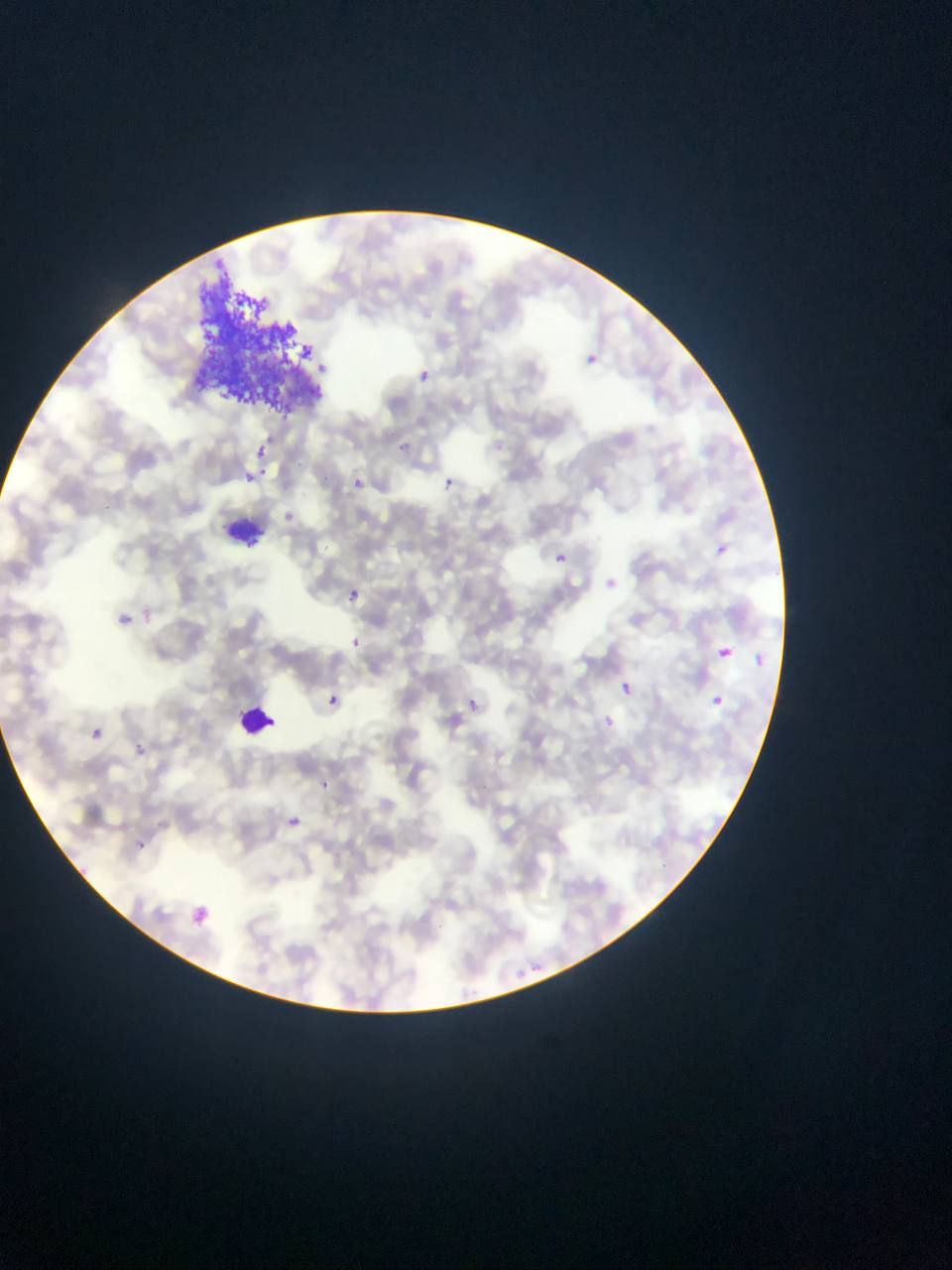
plasmodium_parasite_locations: 'approximate bounding boxes as left top right bottom in pixels: 584 354 601 371; 417 368 432 383; 402 435 419 452; 252 443 269 460; 242 472 257 485; 351 477 363 489; 443 477 454 488; 281 511 298 525; 711 541 730 559; 555 553 568 565; 346 588 361 603; 117 612 127 625; 347 636 363 651; 717 647 730 660; 753 654 767 668; 619 683 633 696; 322 692 344 711; 470 694 486 721; 713 696 724 706; 602 716 614 727; 85 724 106 745; 134 737 151 760; 318 780 346 798; 279 811 307 835; 129 836 150 856; 185 903 213 929'
artifact_stain_precipitate_or_debris_locations: 'approximate bounding boxes as left top right bottom in pixels: 200 271 319 415'
capture: mobile-phone photograph through a microscope
leukocyte_locations: 'approximate bounding boxes as left top right bottom in pixels: 223 511 266 554; 233 699 278 745'
country: Ghana
preparation: thin blood film
field_of_view: single
image_size: 952×1270 pixels